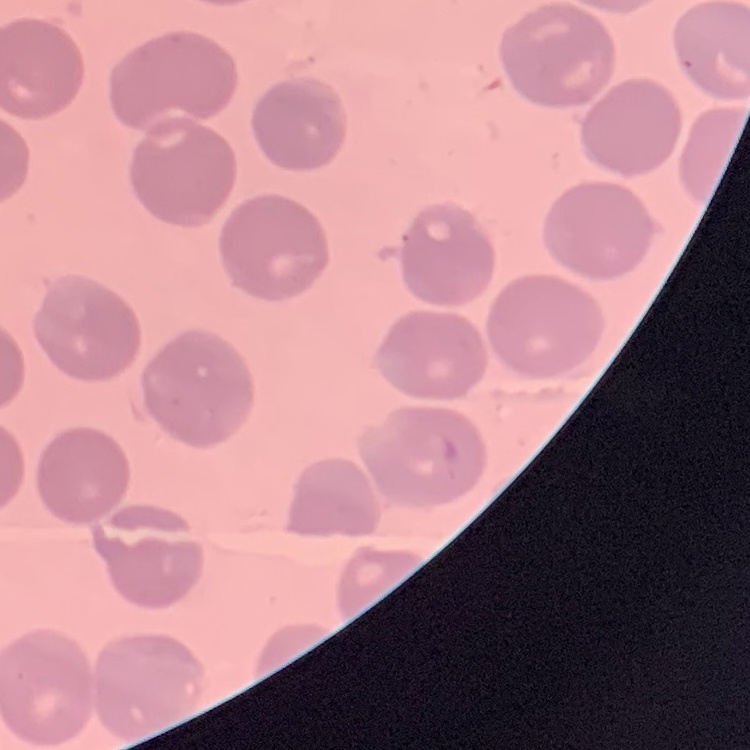
{
  "erythrocyte_morphology": "no rouleaux formation",
  "image_type": "square crop of a larger photomicrograph",
  "preparation": "thin blood smear",
  "stain": "Field's or Giemsa"
}